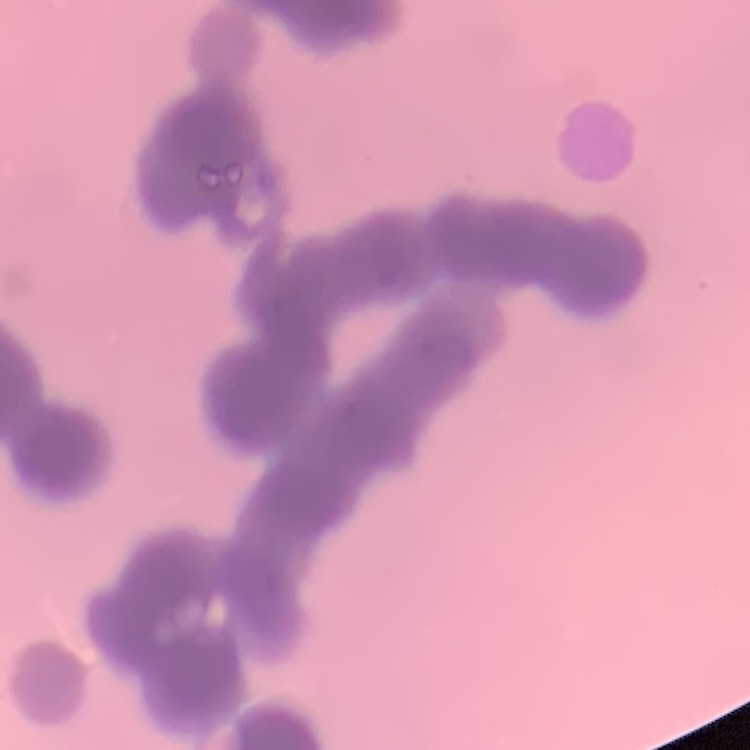
Summary:
  - Red blood cell morphology: rouleaux formation
  - Preparation: thin peripheral smear
  - Stain: Field's or Giemsa
  - Image type: one tile cut from a larger photomicrograph